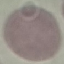

Malaria status: uninfected. Automatically extracted cell patch, resized to 64 × 64 pixels. Acquired by smartphone through the microscope eyepiece. Giemsa stain. Thin smear of blood.